Assess this cell for malaria.
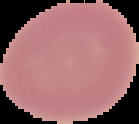
It is uninfected.

Summary:
  - Image type: cell region segmented out of the field of view; surrounding area masked to black
  - Preparation: thin blood film
  - Image size: 139×124 pixels